Name the parasite shown.
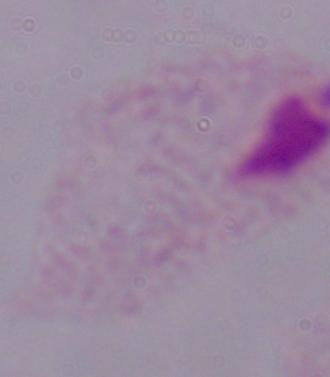

This is a trichomonad.

Photomicrograph. 1000x magnification.